Identify the blood parasite species.
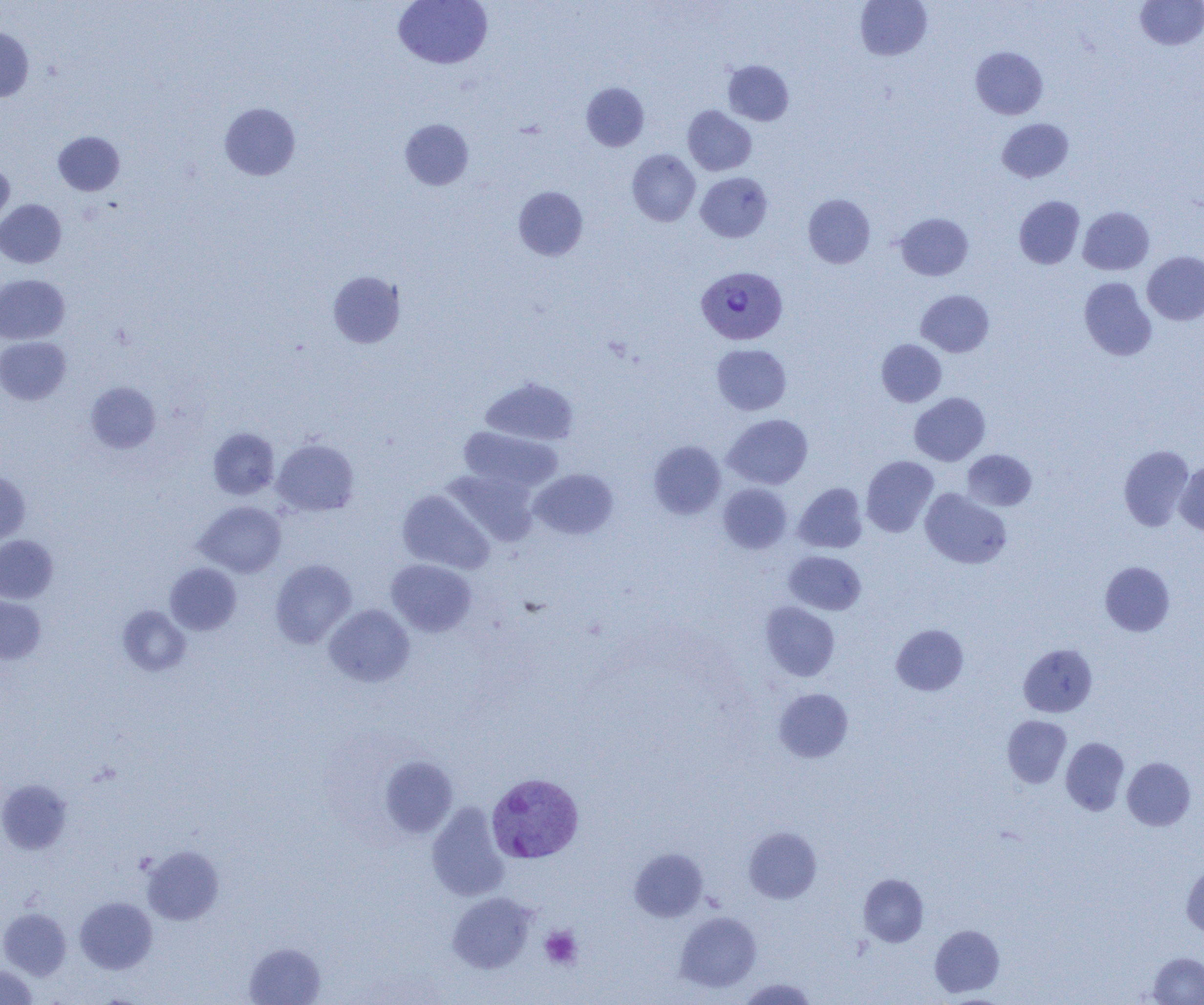
Plasmodium vivax.

Summary:
  - Coordinate format: approximate bounding boxes as [x1, y1, x2, y2] in pixels
  - Platelet locations: [540, 926, 582, 969]
  - Plasmodium vivax-infected red blood cell locations: [696, 264, 787, 344], [486, 773, 584, 864]
  - Uninfected red blood cell locations: [393, 0, 492, 69], [855, 0, 932, 60], [1135, 1, 1204, 50], [0, 27, 33, 102], [970, 46, 1048, 119], [723, 60, 794, 126], [581, 82, 649, 151], [219, 102, 300, 180], [683, 105, 756, 175], [997, 118, 1074, 182], [400, 119, 474, 190], [53, 131, 125, 196], [627, 149, 701, 226], [0, 160, 14, 230], [695, 172, 773, 242], [513, 186, 588, 260], [803, 194, 875, 268], [1014, 196, 1085, 269], [0, 199, 66, 268], [1078, 207, 1154, 275], [895, 213, 973, 280], [1142, 251, 1204, 325], [328, 271, 405, 348], [0, 274, 70, 344], [1079, 277, 1157, 361], [916, 290, 994, 357], [0, 337, 71, 404], [877, 339, 946, 406], [712, 344, 791, 415], [480, 376, 580, 446], [86, 381, 161, 453], [909, 393, 990, 466], [723, 414, 813, 489], [208, 427, 279, 500], [458, 427, 563, 493], [272, 439, 359, 516], [649, 441, 726, 519], [1119, 445, 1195, 531], [962, 449, 1037, 511], [861, 455, 938, 537], [1175, 461, 1204, 535], [444, 469, 539, 546], [530, 469, 618, 540], [0, 470, 30, 545], [794, 482, 867, 553], [718, 483, 792, 554], [920, 488, 1012, 569], [397, 490, 494, 574], [194, 501, 286, 577], [0, 535, 58, 603], [784, 551, 866, 615], [270, 559, 356, 648], [386, 559, 476, 636], [1100, 561, 1175, 636], [165, 563, 242, 635], [0, 596, 46, 664], [761, 602, 840, 681], [324, 604, 415, 687], [117, 605, 191, 676], [891, 624, 968, 695], [1018, 643, 1097, 717], [774, 688, 853, 762], [1002, 715, 1071, 787], [1061, 737, 1129, 815], [379, 754, 457, 839], [1122, 756, 1196, 831], [0, 779, 72, 855], [426, 803, 509, 901], [743, 827, 822, 904], [142, 845, 224, 924], [629, 847, 708, 921], [1181, 864, 1204, 938], [858, 873, 929, 947], [447, 892, 536, 973], [75, 897, 157, 974], [0, 908, 71, 979], [675, 912, 762, 992], [929, 924, 1004, 997], [244, 942, 326, 1005], [1147, 951, 1204, 1004], [0, 964, 38, 1005], [737, 977, 817, 1004]
  - Modality: light microscopy
  - Preparation: thin blood film
  - Field of view: one of a larger specimen
  - Image size: 1204×1005 pixels
  - Magnification: 1000x